Give the extent of all uninfected red blood cells.
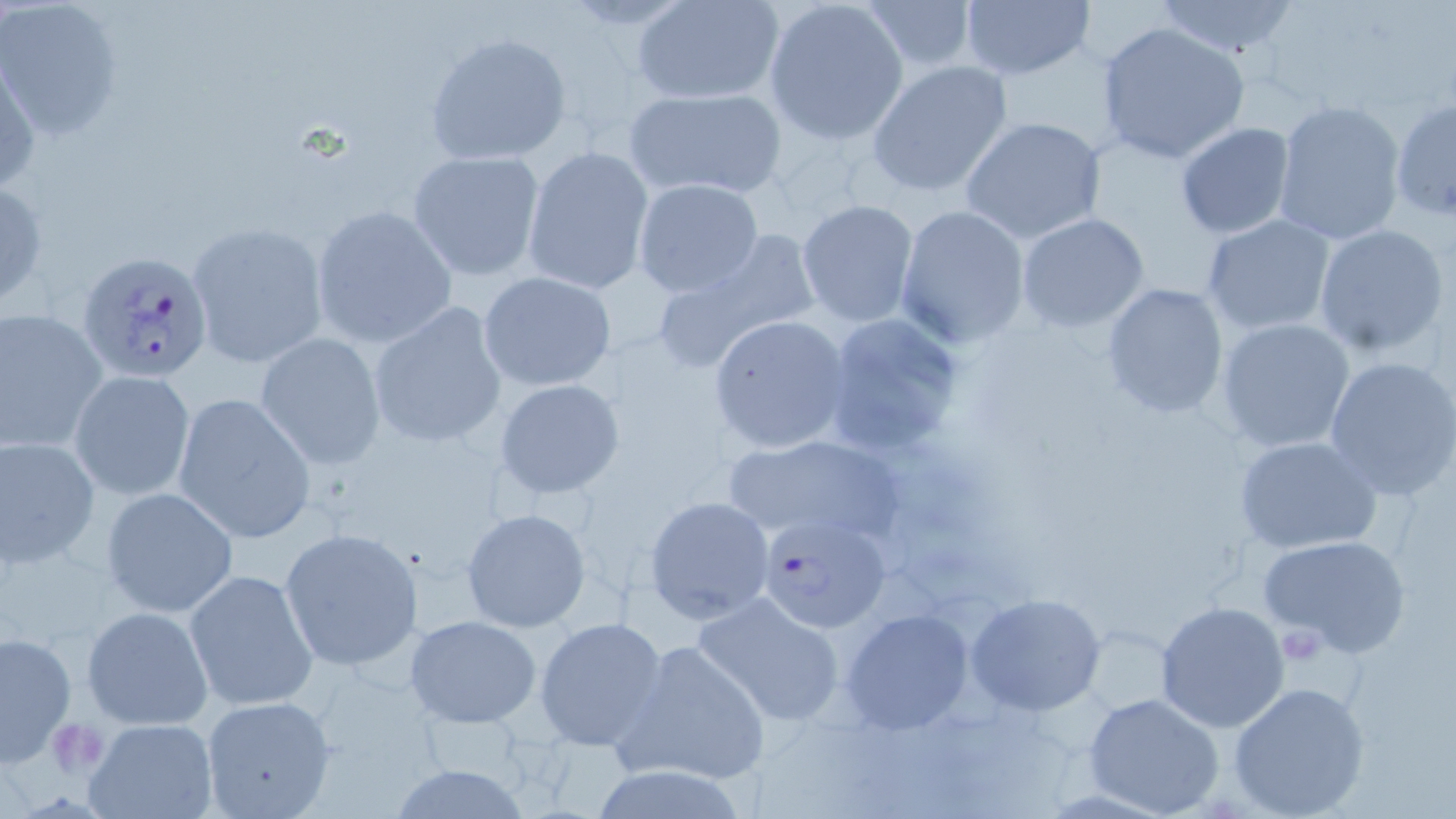

Approximate bounding boxes as (x1,y1)-(x2,y2) corner pairs in pixels.
Uninfected red blood cells: (763,0)-(910,146), (860,0)-(978,72), (957,0)-(1095,82), (1150,0)-(1304,61), (1,1)-(125,143), (633,1)-(787,105), (1096,21)-(1251,165), (424,31)-(571,166), (1,53)-(42,198), (867,61)-(1012,197), (625,86)-(786,200), (1270,98)-(1406,246), (1390,98)-(1456,221), (960,116)-(1107,245), (1174,123)-(1294,240), (522,145)-(654,295), (408,150)-(545,281), (0,177)-(49,312), (632,179)-(765,298), (796,200)-(920,327), (310,203)-(456,348), (895,204)-(1031,348), (1016,213)-(1150,332), (1201,214)-(1335,336), (186,221)-(328,370), (1313,224)-(1451,359), (649,231)-(820,371), (478,270)-(617,391), (1099,281)-(1229,419), (366,301)-(508,448), (1,307)-(106,454), (823,311)-(967,459), (707,314)-(851,453), (1215,317)-(1356,453), (254,330)-(386,469), (1324,355)-(1456,500), (69,370)-(199,503), (494,379)-(625,498), (172,392)-(316,544), (726,433)-(897,544), (0,434)-(100,571), (1233,435)-(1384,556), (100,487)-(239,617), (643,494)-(776,624), (460,506)-(591,633), (279,528)-(423,674), (1256,533)-(1413,659), (184,569)-(316,712), (692,591)-(848,728), (967,593)-(1105,716), (1155,600)-(1290,733), (82,605)-(213,730), (840,607)-(976,736), (406,615)-(543,728), (535,617)-(667,750), (1077,621)-(1179,719), (0,630)-(76,767), (614,640)-(771,787), (1226,682)-(1372,818), (1083,692)-(1224,817), (199,694)-(335,817), (82,717)-(220,819).

slide-level diagnosis = Plasmodium falciparum
preparation = thin blood film
modality = light microscopy
image size = 1456×819 pixels
stain = May-Grünwald-Giemsa
platelet locations = approximate bounding boxes as (x1,y1)-(x2,y2) corner pairs in pixels: (1278,623)-(1326,664), (46,720)-(108,777)
field of view = one of a larger specimen
Plasmodium falciparum-infected red blood cell locations = approximate bounding boxes as (x1,y1)-(x2,y2) corner pairs in pixels: (78,247)-(215,385), (755,512)-(893,634)
magnification = 1000x